Identify the parasite.
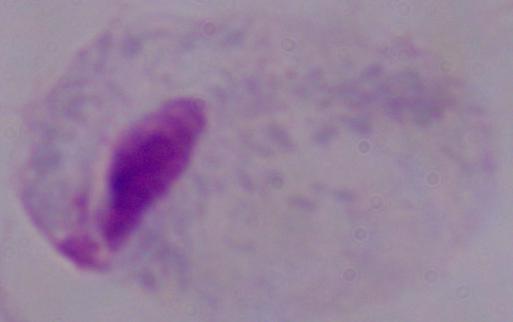
A trichomonad.

magnification = 1000x
modality = photomicrograph